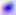
Summary:
  - Magnification: 400x
  - Modality: photomicrograph
  - Identification: Toxoplasma gondii